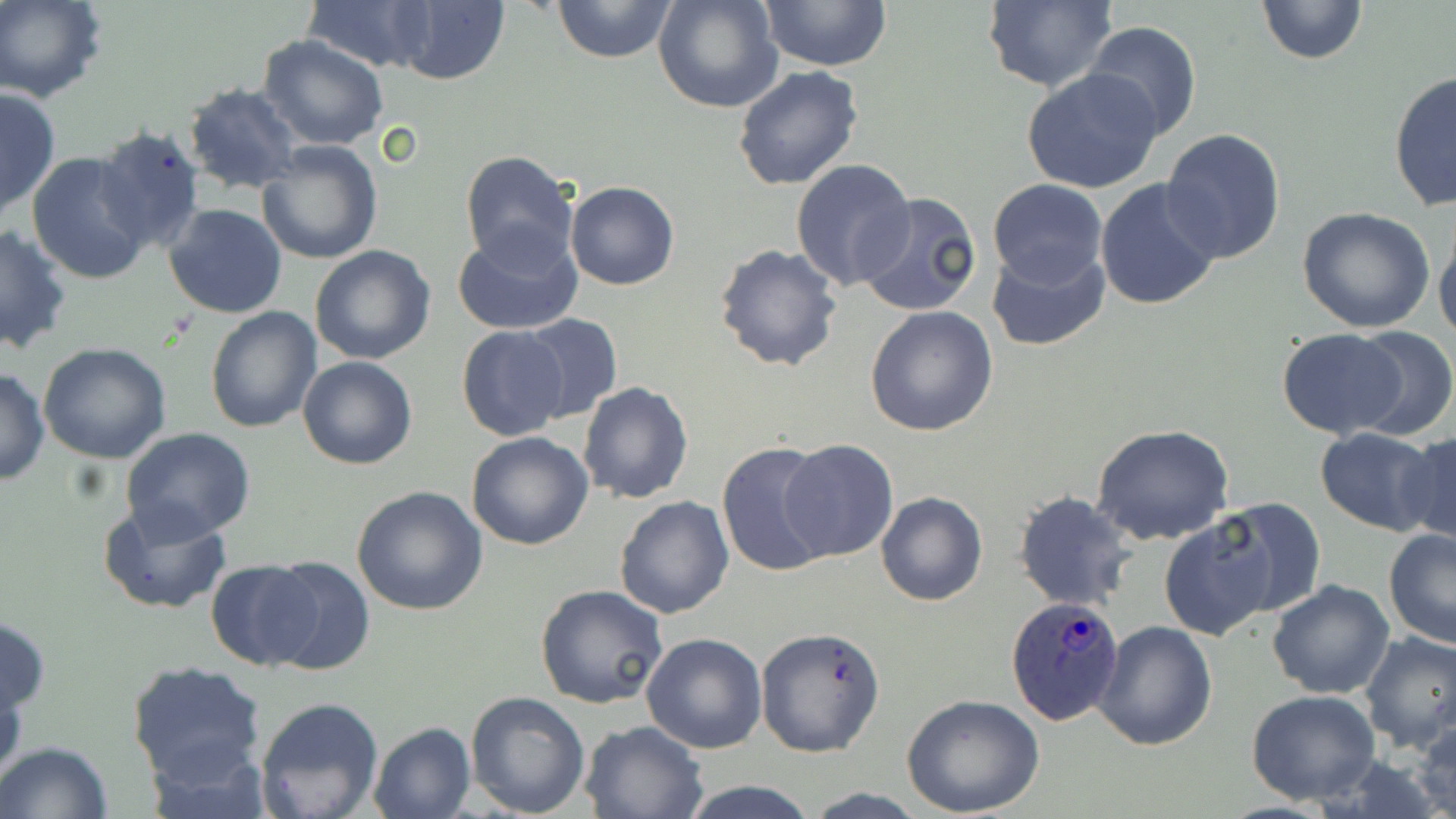

Summary:
  - Coordinate format: approximate bounding boxes as (x1,y1)-(x2,y2) corner pairs in pixels
  - Uninfected red blood cell locations: (1,0)-(107,103), (303,0)-(442,73), (552,0)-(677,63), (652,0)-(784,114), (1255,0)-(1368,65), (979,1)-(1117,92), (388,2)-(510,85), (760,2)-(890,71), (1083,21)-(1203,142), (256,36)-(389,151), (731,65)-(864,192), (1022,68)-(1163,195), (1387,71)-(1455,212), (182,82)-(304,196), (1,85)-(59,219), (94,123)-(207,253), (1161,128)-(1286,264), (257,142)-(382,264), (459,151)-(578,271), (27,152)-(154,285), (790,158)-(915,291), (988,178)-(1108,289), (1095,178)-(1222,313), (565,180)-(680,291), (855,193)-(984,319), (164,203)-(289,317), (1295,206)-(1436,333), (1434,223)-(1456,348), (0,225)-(73,357), (453,226)-(585,334), (714,242)-(843,372), (310,245)-(437,366), (986,245)-(1110,352), (864,304)-(998,435), (205,305)-(323,432), (515,312)-(623,424), (1341,325)-(1456,442), (456,326)-(571,442), (1276,328)-(1411,440), (37,344)-(171,464), (298,356)-(418,471), (0,367)-(49,486), (577,383)-(693,504), (1090,424)-(1235,547), (121,428)-(257,542), (1314,428)-(1440,534), (466,430)-(596,550), (1399,430)-(1456,549), (779,438)-(899,564), (715,441)-(835,579), (352,484)-(487,615), (1013,491)-(1136,611), (875,492)-(989,607), (614,495)-(734,619), (99,499)-(232,616), (1207,499)-(1325,618), (1159,514)-(1280,641), (1383,528)-(1456,649), (262,556)-(374,675), (206,558)-(321,669), (1267,579)-(1396,698), (535,583)-(669,709), (0,613)-(52,722), (1095,621)-(1219,752), (755,626)-(886,759), (1358,630)-(1456,752), (641,632)-(767,753), (126,659)-(269,790), (0,664)-(27,790), (1246,689)-(1382,805), (465,691)-(590,818), (900,695)-(1046,818), (254,697)-(385,819), (580,719)-(708,818), (1410,719)-(1456,819), (368,721)-(475,819), (0,742)-(115,819), (676,781)-(824,818)
  - Plasmodium ovale-infected red blood cell locations: (1006,597)-(1126,725)
  - Slide-level diagnosis: Plasmodium ovale
  - Image size: 1456×819 pixels
  - Field of view: single
  - Magnification: 1000x
  - Modality: optical microscopy
  - Preparation: thin blood smear
  - Stain: May-Grünwald-Giemsa